Name the parasite shown.
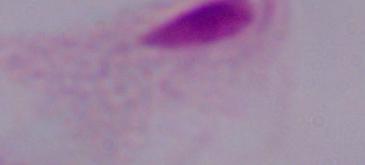
A trichomonad.

Micrograph. 1000x magnification.